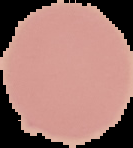
image size = 133×148 pixels
preparation = thin blood film
malaria status = uninfected
image type = segmented cell region with the area outside set to black